Locate and identify every blood parasite.
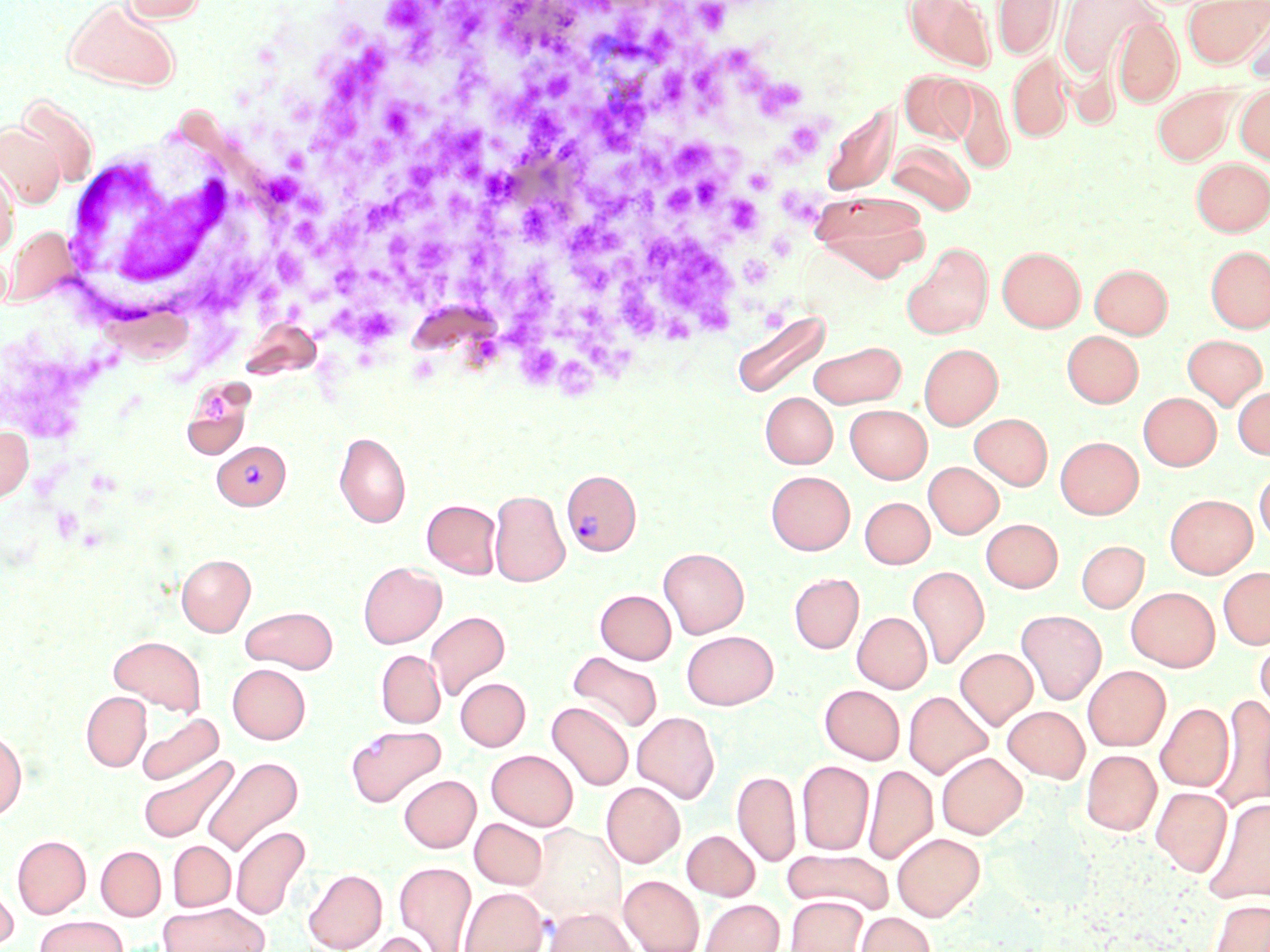

Approximate bounding boxes as (x1, y1, x2, y2) in pixels.
Plasmodium vivax-infected red blood cells: (212, 439, 290, 510), (560, 468, 642, 556).
No Plasmodium falciparum, Plasmodium ovale, Plasmodium malariae, Babesia divergens, or Trypanosoma brucei observed.

White blood cell locations: (56, 124, 283, 337). Uninfected red blood cell locations: (121, 0, 207, 23), (904, 0, 995, 70), (992, 0, 1062, 60), (1057, 0, 1156, 78), (1183, 0, 1268, 68), (64, 1, 180, 91), (1242, 5, 1270, 83), (1112, 16, 1183, 107), (1007, 51, 1073, 142), (899, 70, 974, 143), (948, 78, 1014, 173), (1234, 82, 1270, 164), (1153, 85, 1238, 165), (15, 94, 99, 188), (821, 102, 898, 197), (1, 122, 65, 209), (887, 141, 975, 214), (1191, 157, 1270, 235), (0, 163, 19, 255), (813, 192, 930, 279), (3, 226, 77, 306), (902, 243, 993, 339), (1206, 245, 1270, 333), (997, 247, 1085, 332), (1090, 264, 1172, 338), (731, 309, 831, 399), (1062, 330, 1143, 407), (1182, 334, 1267, 409), (809, 341, 906, 408), (919, 343, 1003, 429), (182, 380, 255, 455), (1233, 386, 1270, 459), (761, 392, 837, 468), (1138, 392, 1221, 470), (845, 404, 932, 483), (969, 413, 1052, 490), (0, 424, 34, 503), (335, 432, 410, 528), (1055, 436, 1143, 519), (923, 462, 1003, 539), (1254, 464, 1270, 546), (766, 471, 854, 554), (489, 489, 570, 587), (1165, 493, 1257, 578), (860, 497, 934, 568), (422, 499, 501, 578), (981, 518, 1063, 592), (1076, 540, 1149, 613), (658, 547, 749, 638), (176, 554, 255, 636), (358, 562, 446, 648), (907, 566, 990, 669), (1217, 566, 1270, 649), (789, 573, 863, 653), (1126, 586, 1220, 671), (595, 589, 676, 664), (241, 606, 337, 673), (1016, 609, 1106, 705), (425, 610, 510, 700), (852, 612, 931, 693), (681, 630, 779, 709), (1254, 632, 1270, 721), (108, 635, 206, 715), (955, 648, 1037, 729), (376, 650, 445, 728), (567, 651, 664, 734), (227, 664, 310, 744), (1083, 665, 1170, 751), (455, 677, 530, 751), (820, 684, 905, 764), (904, 690, 993, 779), (81, 692, 151, 771), (1211, 694, 1270, 812), (547, 701, 634, 791), (1156, 703, 1233, 791), (1003, 706, 1090, 782), (632, 711, 719, 802), (137, 713, 223, 785), (346, 725, 446, 806), (0, 728, 27, 821), (1081, 749, 1161, 835), (486, 750, 578, 830), (936, 752, 1027, 838), (137, 754, 239, 843), (202, 755, 304, 856), (797, 760, 874, 855), (863, 764, 937, 865), (733, 769, 801, 867), (399, 775, 480, 852), (601, 781, 685, 867), (1151, 786, 1232, 876), (1203, 797, 1270, 904), (470, 818, 548, 890), (526, 823, 625, 924), (231, 826, 310, 920), (682, 830, 760, 900), (892, 832, 985, 920), (12, 835, 90, 918), (167, 841, 235, 911), (96, 846, 165, 920), (782, 849, 894, 914), (394, 861, 477, 952), (304, 869, 387, 951), (0, 874, 18, 951), (619, 875, 704, 952), (459, 887, 548, 952), (786, 896, 867, 952), (698, 898, 784, 952), (1209, 899, 1270, 952), (158, 902, 270, 952), (544, 906, 637, 952), (856, 912, 935, 952), (35, 915, 127, 952), (365, 931, 439, 952). Platelet locations: (386, 0, 430, 33), (442, 2, 496, 51), (697, 2, 732, 33), (646, 25, 683, 66), (330, 43, 397, 107), (731, 46, 764, 80), (689, 48, 728, 110), (451, 49, 497, 107), (655, 65, 690, 106), (544, 70, 578, 107), (752, 78, 805, 119), (296, 93, 364, 159), (592, 95, 653, 158), (380, 96, 419, 141), (517, 107, 572, 161), (431, 124, 490, 185), (786, 124, 821, 156), (669, 139, 715, 176), (641, 144, 672, 185), (410, 156, 445, 199), (739, 164, 775, 196), (266, 168, 309, 209), (692, 172, 726, 213), (663, 181, 698, 217), (584, 182, 660, 218), (787, 184, 823, 224), (360, 186, 426, 233), (728, 194, 760, 234), (515, 204, 557, 249), (566, 212, 633, 263), (287, 214, 329, 250), (644, 228, 736, 336), (382, 230, 420, 287), (413, 237, 457, 274), (272, 245, 314, 290), (739, 252, 782, 289), (500, 257, 558, 348), (330, 258, 367, 300), (572, 259, 612, 293), (617, 296, 662, 338), (560, 303, 633, 376), (332, 305, 399, 347), (478, 338, 500, 362), (523, 343, 564, 384), (555, 353, 598, 400), (204, 394, 230, 421). Slide-level diagnosis: Plasmodium vivax. 1000x magnification. One field of a larger specimen. Thin blood smear. May-Grünwald-Giemsa-stained preparation. Light microscopy. Image is 1270×952 pixels.